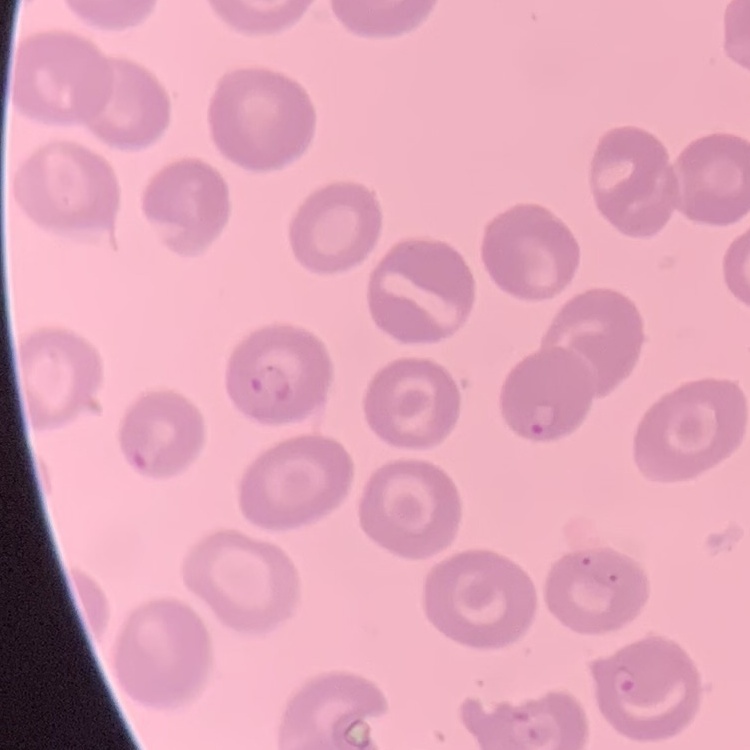

Summary:
  - Erythrocyte morphology: no rouleaux formation
  - Stain: Field's or Giemsa
  - Image type: square crop of a larger photomicrograph
  - Preparation: thin blood smear